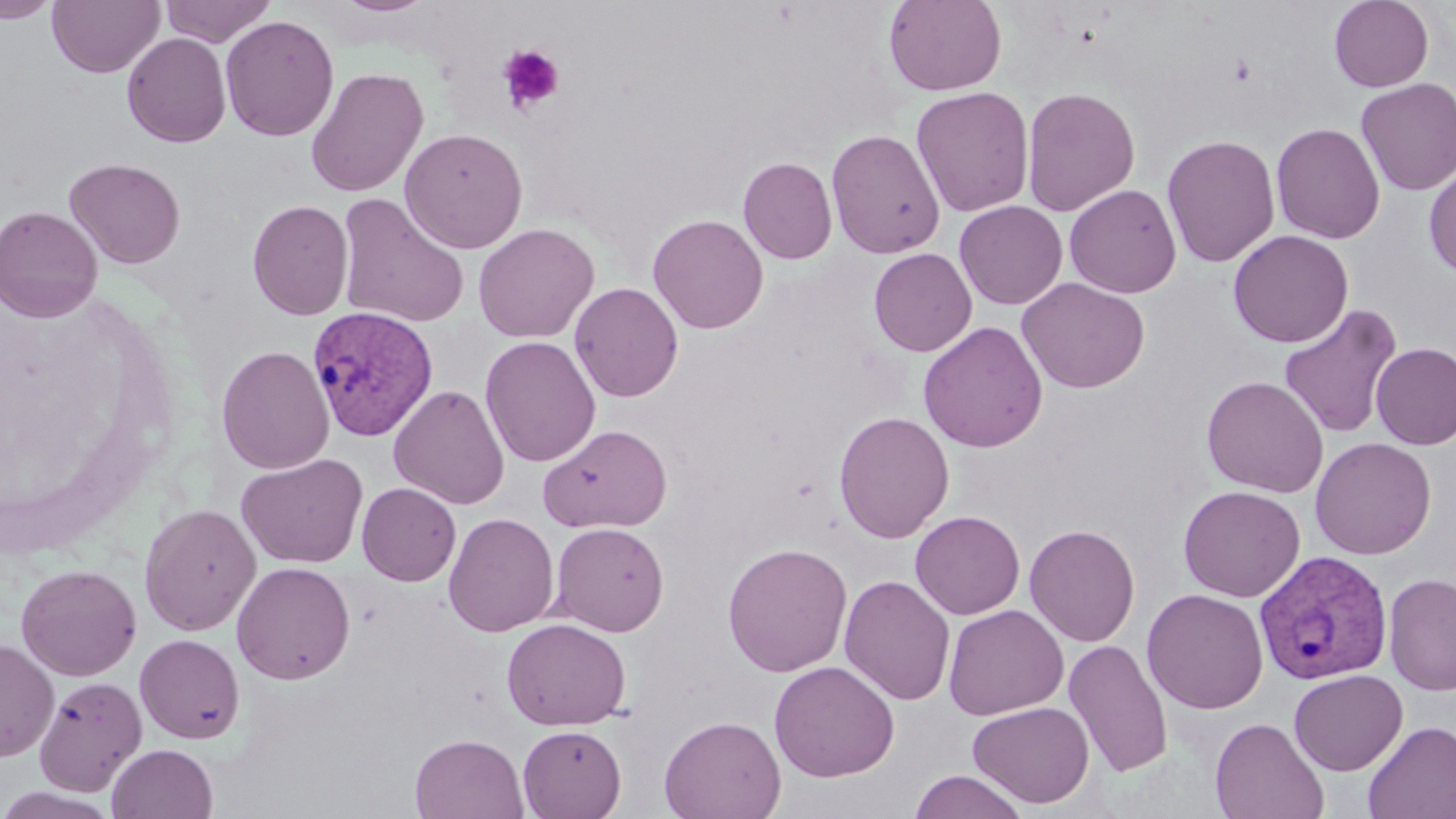
Approximate bounding boxes as named x1/y1/x2/y2 corners in pixels. Plasmodium vivax-infected red blood cell locations: (x1=308, y1=306, x2=440, y2=441), (x1=1254, y1=549, x2=1393, y2=685). Uninfected red blood cell locations: (x1=0, y1=0, x2=60, y2=22), (x1=47, y1=0, x2=165, y2=78), (x1=159, y1=0, x2=276, y2=46), (x1=335, y1=0, x2=434, y2=15), (x1=884, y1=0, x2=1007, y2=96), (x1=1329, y1=0, x2=1434, y2=92), (x1=220, y1=15, x2=340, y2=142), (x1=122, y1=32, x2=232, y2=147), (x1=304, y1=67, x2=429, y2=198), (x1=1355, y1=78, x2=1456, y2=197), (x1=911, y1=86, x2=1034, y2=218), (x1=1020, y1=86, x2=1141, y2=217), (x1=1271, y1=122, x2=1385, y2=244), (x1=399, y1=127, x2=528, y2=254), (x1=825, y1=129, x2=945, y2=259), (x1=1161, y1=133, x2=1281, y2=268), (x1=738, y1=156, x2=838, y2=264), (x1=64, y1=158, x2=186, y2=269), (x1=1423, y1=161, x2=1456, y2=277), (x1=1064, y1=184, x2=1182, y2=298), (x1=335, y1=193, x2=471, y2=328), (x1=247, y1=199, x2=354, y2=320), (x1=954, y1=200, x2=1068, y2=309), (x1=0, y1=205, x2=103, y2=322), (x1=648, y1=213, x2=768, y2=334), (x1=473, y1=223, x2=599, y2=343), (x1=1228, y1=229, x2=1353, y2=348), (x1=869, y1=248, x2=977, y2=356), (x1=1017, y1=277, x2=1150, y2=394), (x1=569, y1=282, x2=683, y2=402), (x1=1278, y1=304, x2=1402, y2=439), (x1=918, y1=321, x2=1048, y2=453), (x1=480, y1=335, x2=600, y2=468), (x1=1371, y1=342, x2=1456, y2=449), (x1=216, y1=344, x2=335, y2=474), (x1=1201, y1=375, x2=1328, y2=498), (x1=389, y1=384, x2=510, y2=510), (x1=833, y1=410, x2=955, y2=544), (x1=540, y1=423, x2=672, y2=532), (x1=1310, y1=436, x2=1436, y2=560), (x1=236, y1=453, x2=368, y2=569), (x1=357, y1=482, x2=461, y2=586), (x1=1178, y1=485, x2=1306, y2=601), (x1=139, y1=503, x2=261, y2=636), (x1=910, y1=510, x2=1025, y2=619), (x1=443, y1=512, x2=559, y2=637), (x1=550, y1=522, x2=670, y2=636), (x1=1024, y1=523, x2=1140, y2=647), (x1=721, y1=542, x2=853, y2=677), (x1=231, y1=561, x2=356, y2=684), (x1=15, y1=563, x2=142, y2=681), (x1=1384, y1=572, x2=1456, y2=696), (x1=839, y1=575, x2=956, y2=706), (x1=1142, y1=588, x2=1269, y2=714), (x1=943, y1=604, x2=1068, y2=720), (x1=501, y1=617, x2=631, y2=731), (x1=135, y1=633, x2=245, y2=743), (x1=0, y1=638, x2=59, y2=761), (x1=1063, y1=639, x2=1173, y2=777), (x1=769, y1=660, x2=900, y2=782), (x1=1289, y1=669, x2=1408, y2=776), (x1=34, y1=676, x2=148, y2=796), (x1=967, y1=702, x2=1095, y2=808), (x1=658, y1=714, x2=786, y2=819), (x1=1209, y1=717, x2=1329, y2=819), (x1=1363, y1=720, x2=1456, y2=818), (x1=517, y1=724, x2=626, y2=819), (x1=409, y1=733, x2=529, y2=818), (x1=107, y1=743, x2=218, y2=819), (x1=908, y1=769, x2=1029, y2=819), (x1=0, y1=787, x2=119, y2=819). Platelet locations: (x1=498, y1=45, x2=564, y2=115). Slide-level diagnosis: Plasmodium vivax. 1000x magnification. Thin blood smear. One field of a larger specimen. Image is 1456×819 pixels. Optical microscopy. May-Grünwald-Giemsa-stained preparation.